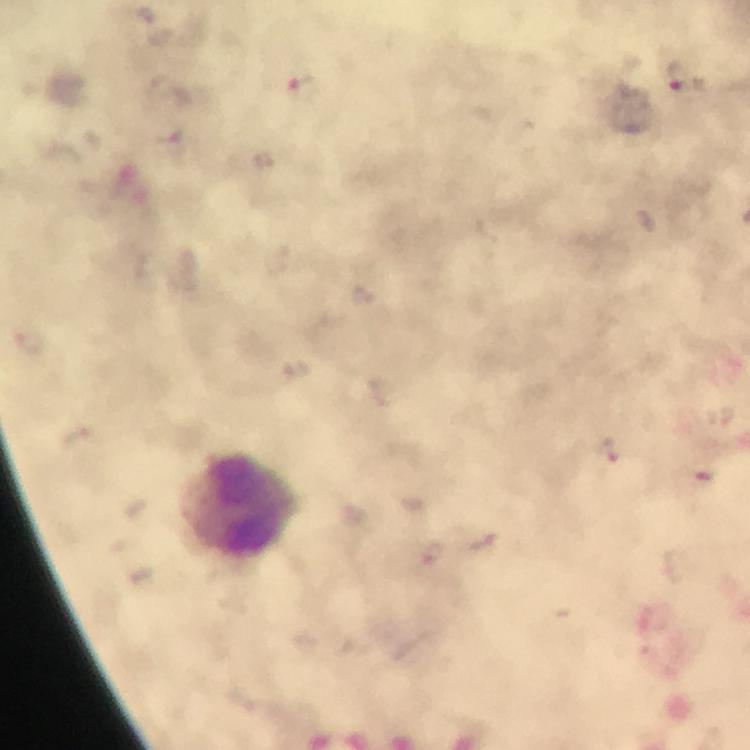

Approximate centers as {x, y} in pixels.
Summary:
  - Leukocyte locations: {236, 507}
  - Plasmodium parasite locations: {676, 75}, {302, 82}, {483, 543}, {432, 553}
  - Magnification: 100x
  - Cropped from: one field of view
  - Capture: smartphone photograph through a microscope
  - Context: from a malaria diagnostic workup
  - Stain: Giemsa
  - Immersion oil: applied
  - Image size: 750×750 pixels
  - Preparation: thick blood smear